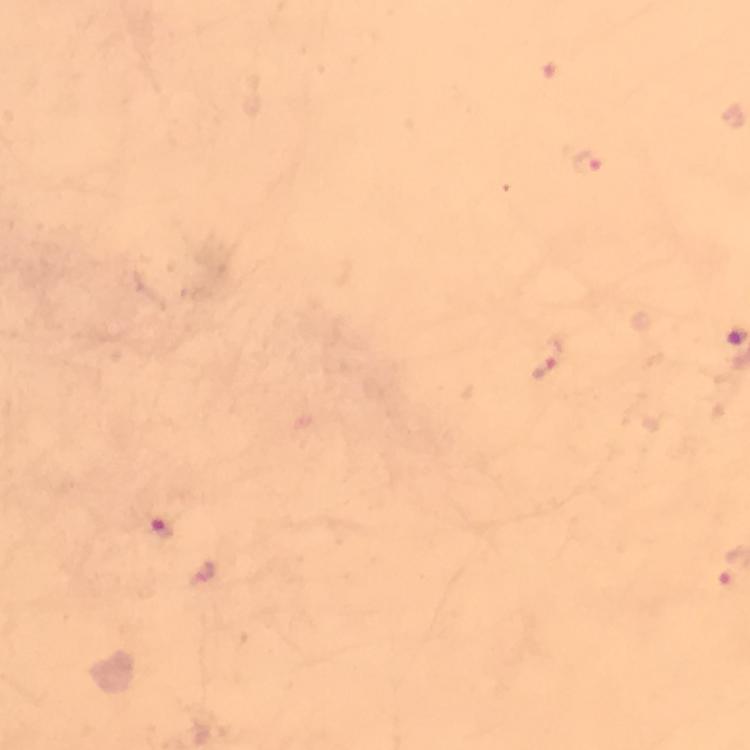

Approximate centers as [x, y] in pixels.
Summary:
  - Malaria parasite locations: [587, 163], [547, 359], [164, 531]
  - Preparation: thick blood smear
  - Stain: Giemsa
  - Magnification: 100x
  - Capture: smartphone camera through the microscope
  - Context: from a malaria diagnostic workup
  - Immersion oil: used
  - Cropped from: a single field of view
  - Image size: 750×750 pixels